Outline each blood parasite and name the species.
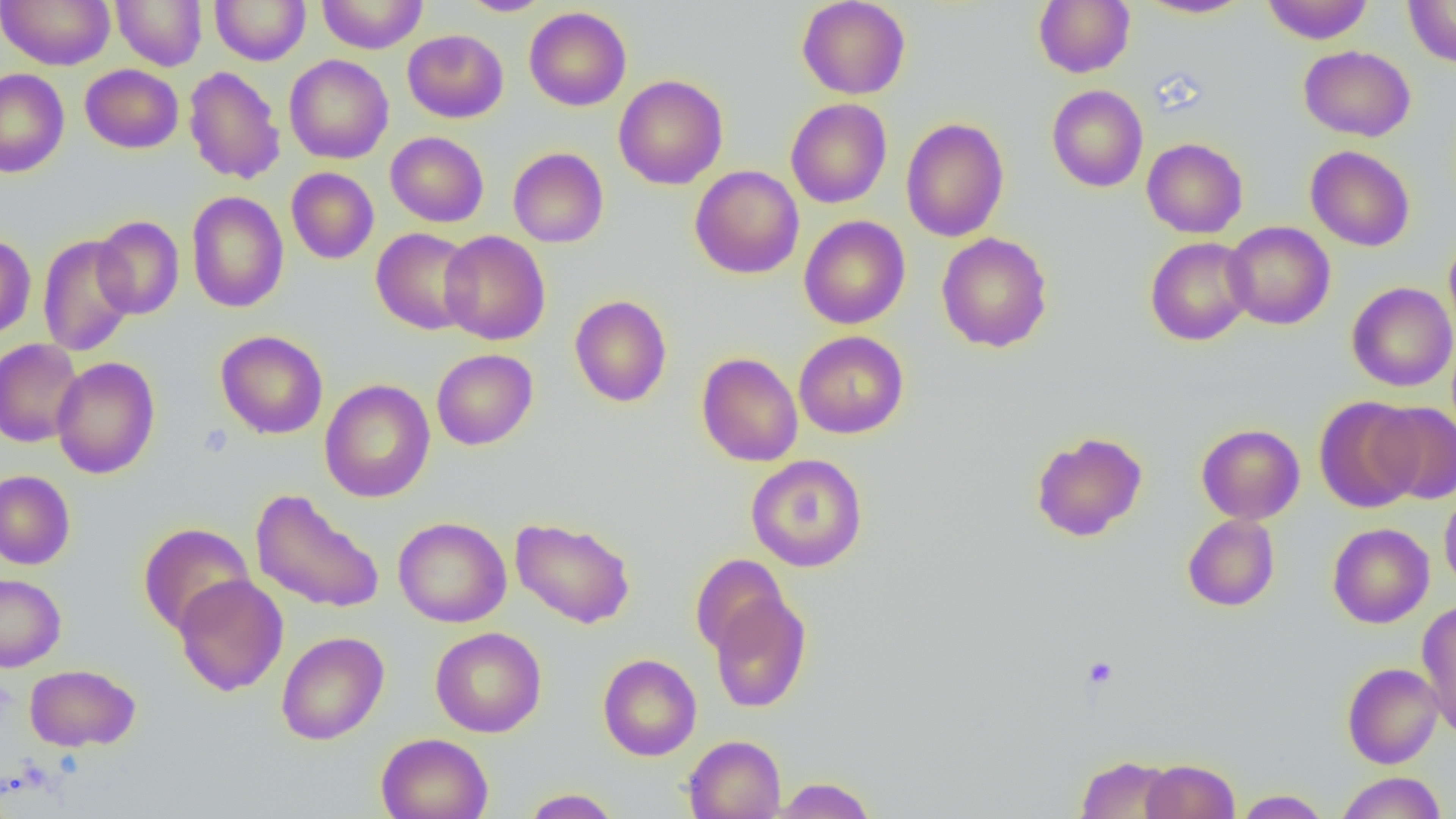

No blood parasites seen.

Summary:
  - Coordinate format: approximate bounding boxes as named x1/y1/x2/y2 corners in pixels
  - Uninfected red blood cell locations: (x1=0, y1=0, x2=115, y2=70), (x1=111, y1=0, x2=207, y2=70), (x1=210, y1=0, x2=311, y2=65), (x1=317, y1=0, x2=428, y2=54), (x1=458, y1=0, x2=554, y2=16), (x1=796, y1=0, x2=910, y2=99), (x1=1034, y1=0, x2=1134, y2=77), (x1=1262, y1=0, x2=1373, y2=44), (x1=1403, y1=0, x2=1456, y2=68), (x1=1138, y1=1, x2=1252, y2=19), (x1=524, y1=7, x2=631, y2=110), (x1=403, y1=29, x2=508, y2=123), (x1=1298, y1=45, x2=1415, y2=141), (x1=284, y1=54, x2=393, y2=164), (x1=80, y1=64, x2=184, y2=154), (x1=184, y1=65, x2=286, y2=185), (x1=0, y1=68, x2=69, y2=178), (x1=614, y1=74, x2=728, y2=190), (x1=1047, y1=84, x2=1148, y2=192), (x1=785, y1=99, x2=892, y2=208), (x1=901, y1=118, x2=1009, y2=242), (x1=386, y1=131, x2=488, y2=227), (x1=1142, y1=138, x2=1248, y2=238), (x1=1305, y1=145, x2=1415, y2=251), (x1=508, y1=147, x2=609, y2=248), (x1=690, y1=165, x2=804, y2=279), (x1=286, y1=167, x2=378, y2=264), (x1=187, y1=191, x2=288, y2=313), (x1=92, y1=215, x2=184, y2=320), (x1=799, y1=215, x2=911, y2=329), (x1=1223, y1=221, x2=1335, y2=329), (x1=371, y1=227, x2=478, y2=335), (x1=439, y1=230, x2=550, y2=345), (x1=0, y1=232, x2=36, y2=340), (x1=936, y1=232, x2=1053, y2=353), (x1=38, y1=234, x2=138, y2=356), (x1=1443, y1=234, x2=1456, y2=342), (x1=1145, y1=237, x2=1255, y2=346), (x1=1347, y1=282, x2=1456, y2=392), (x1=569, y1=295, x2=672, y2=407), (x1=216, y1=330, x2=328, y2=439), (x1=793, y1=331, x2=909, y2=438), (x1=0, y1=339, x2=84, y2=447), (x1=432, y1=348, x2=538, y2=450), (x1=696, y1=352, x2=803, y2=466), (x1=51, y1=356, x2=160, y2=479), (x1=320, y1=379, x2=436, y2=503), (x1=1313, y1=396, x2=1423, y2=513), (x1=1371, y1=401, x2=1456, y2=505), (x1=1196, y1=423, x2=1305, y2=524), (x1=1030, y1=431, x2=1148, y2=542), (x1=746, y1=454, x2=868, y2=572), (x1=0, y1=470, x2=75, y2=570), (x1=250, y1=489, x2=385, y2=614), (x1=1439, y1=490, x2=1456, y2=596), (x1=1182, y1=514, x2=1280, y2=611), (x1=393, y1=517, x2=511, y2=627), (x1=510, y1=517, x2=636, y2=628), (x1=139, y1=522, x2=255, y2=636), (x1=1327, y1=523, x2=1434, y2=628), (x1=690, y1=554, x2=790, y2=658), (x1=0, y1=573, x2=66, y2=672), (x1=173, y1=575, x2=288, y2=696), (x1=710, y1=592, x2=811, y2=713), (x1=1417, y1=600, x2=1456, y2=737), (x1=430, y1=627, x2=546, y2=737), (x1=276, y1=631, x2=389, y2=745), (x1=598, y1=653, x2=701, y2=761), (x1=1342, y1=662, x2=1443, y2=768), (x1=24, y1=664, x2=141, y2=751), (x1=376, y1=732, x2=493, y2=819), (x1=683, y1=735, x2=786, y2=818), (x1=1076, y1=755, x2=1177, y2=818), (x1=1141, y1=758, x2=1240, y2=819), (x1=1335, y1=771, x2=1448, y2=819), (x1=771, y1=776, x2=876, y2=818), (x1=520, y1=788, x2=622, y2=818), (x1=1233, y1=789, x2=1331, y2=818)
  - Platelet locations: (x1=198, y1=424, x2=233, y2=457), (x1=1081, y1=655, x2=1119, y2=690)
  - Slide-level diagnosis: negative for blood parasites
  - Modality: light microscopy
  - Image size: 1456×819 pixels
  - Magnification: 1000x
  - Preparation: thin blood film
  - Field of view: single